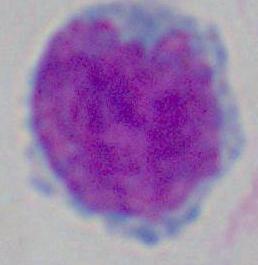
Summary:
  - Modality: micrograph
  - Identification: white blood cell
  - Magnification: 1000x